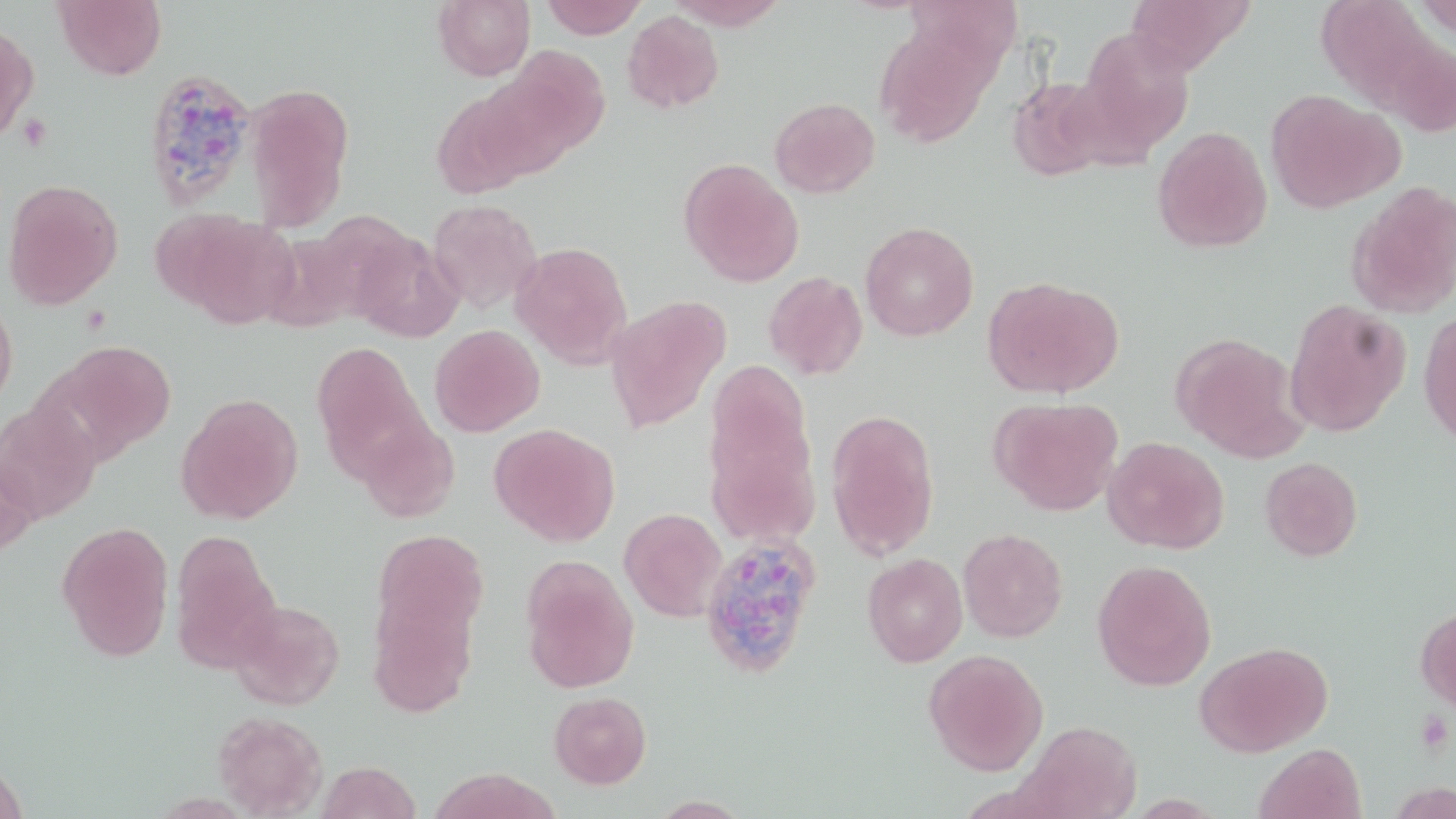
slide_level_diagnosis: Plasmodium ovale
image_size: 1456×819 pixels
plasmodium_ovale_infected_red_blood_cell_locations: 'approximate bounding boxes as (x1,y1)-(x2,y2) corner pairs in pixels: (141,68)-(258,208), (699,534)-(823,678)'
stain: May-Grünwald-Giemsa
platelet_locations: 'approximate bounding boxes as (x1,y1)-(x2,y2) corner pairs in pixels: (16,114)-(53,151), (1415,711)-(1452,754)'
modality: optical microscopy
preparation: thin blood smear
field_of_view: one of a larger specimen
magnification: 1000x
uninfected_red_blood_cell_locations: 'approximate bounding boxes as (x1,y1)-(x2,y2) corner pairs in pixels: (53,0)-(166,79), (432,0)-(535,81), (540,0)-(647,39), (666,0)-(789,30), (1125,0)-(1253,75), (622,10)-(725,114), (873,20)-(1000,147), (0,22)-(40,144), (1076,28)-(1196,158), (486,48)-(610,172), (1006,76)-(1113,182), (246,84)-(352,228), (1265,89)-(1404,214), (769,97)-(880,198), (1152,126)-(1273,253), (679,158)-(804,287), (2,179)-(124,310), (1346,180)-(1456,320), (427,199)-(542,313), (171,213)-(299,329), (860,221)-(979,341), (349,233)-(463,343), (510,241)-(633,367), (763,271)-(868,380), (982,276)-(1123,400), (604,295)-(730,434), (1284,298)-(1411,437), (0,300)-(18,410), (1418,308)-(1456,447), (429,324)-(545,437), (1170,332)-(1305,461), (55,340)-(176,457), (311,341)-(428,478), (704,365)-(819,533), (175,393)-(305,525), (988,396)-(1124,516), (0,403)-(102,524), (826,409)-(940,560), (357,420)-(460,523), (489,424)-(620,547), (1102,436)-(1230,554), (0,451)-(38,562), (1259,456)-(1363,561), (619,507)-(728,622), (56,521)-(174,661), (958,528)-(1068,643), (371,531)-(490,641), (169,533)-(282,673), (862,553)-(968,667), (520,556)-(639,694), (1092,559)-(1217,691), (367,589)-(480,719), (229,599)-(345,709), (1414,603)-(1456,714), (1194,640)-(1334,758), (923,649)-(1049,776), (549,691)-(652,789), (211,711)-(328,817), (1017,720)-(1141,818), (1254,742)-(1367,819), (0,759)-(30,819), (316,761)-(422,819), (426,768)-(560,818)'